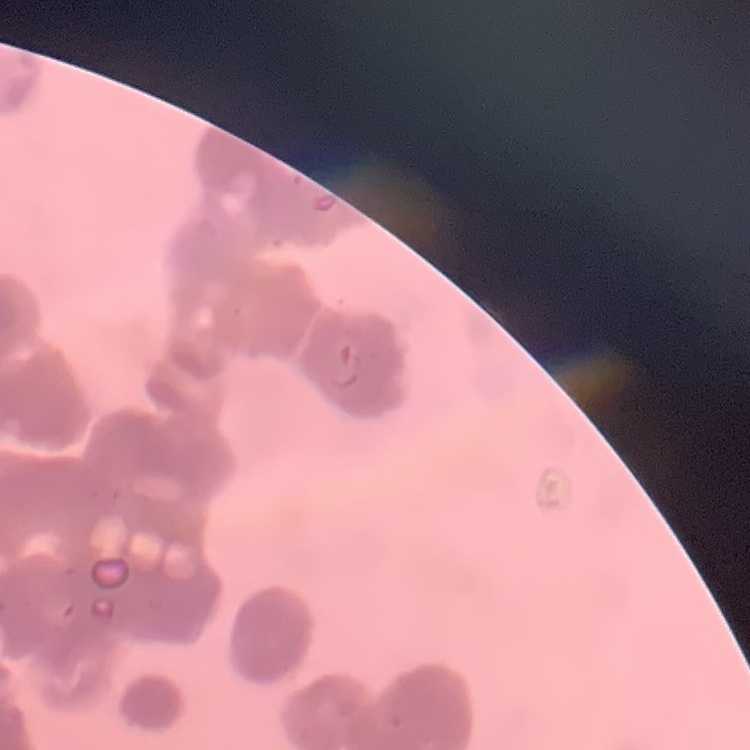

{
  "erythrocyte_morphology": "rouleaux formation",
  "preparation": "thin peripheral smear",
  "stain": "Field's or Giemsa",
  "image_type": "square crop of a larger photomicrograph"
}